Assess this cell for malaria.
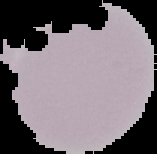

Uninfected.

From a thin blood film. Cell region segmented out of the field of view; the surrounding area is masked to black. Image is 157×154 pixels.